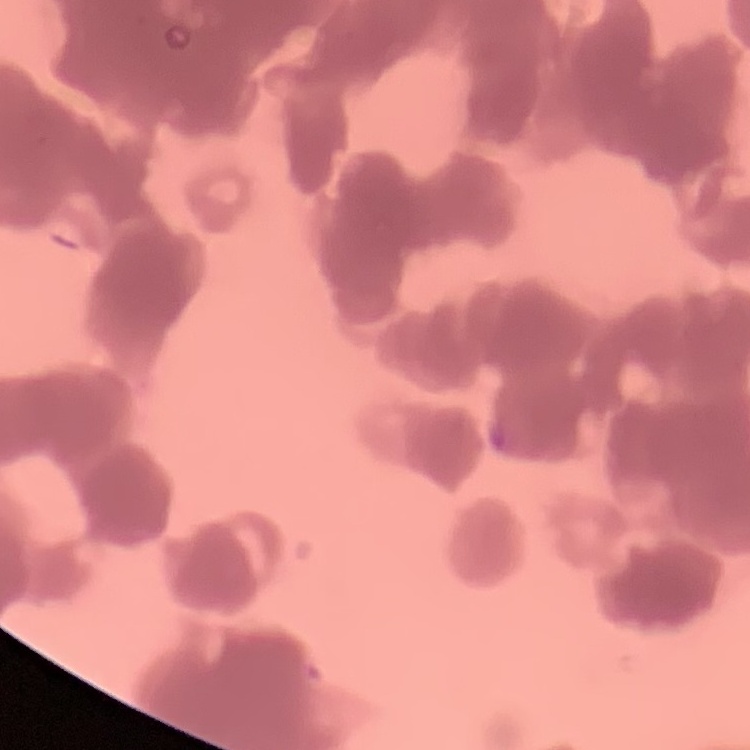

Summary:
  - Erythrocyte morphology: rouleaux formation
  - Preparation: thin peripheral smear
  - Image type: one tile cut from a larger photomicrograph
  - Stain: Field's or Giemsa